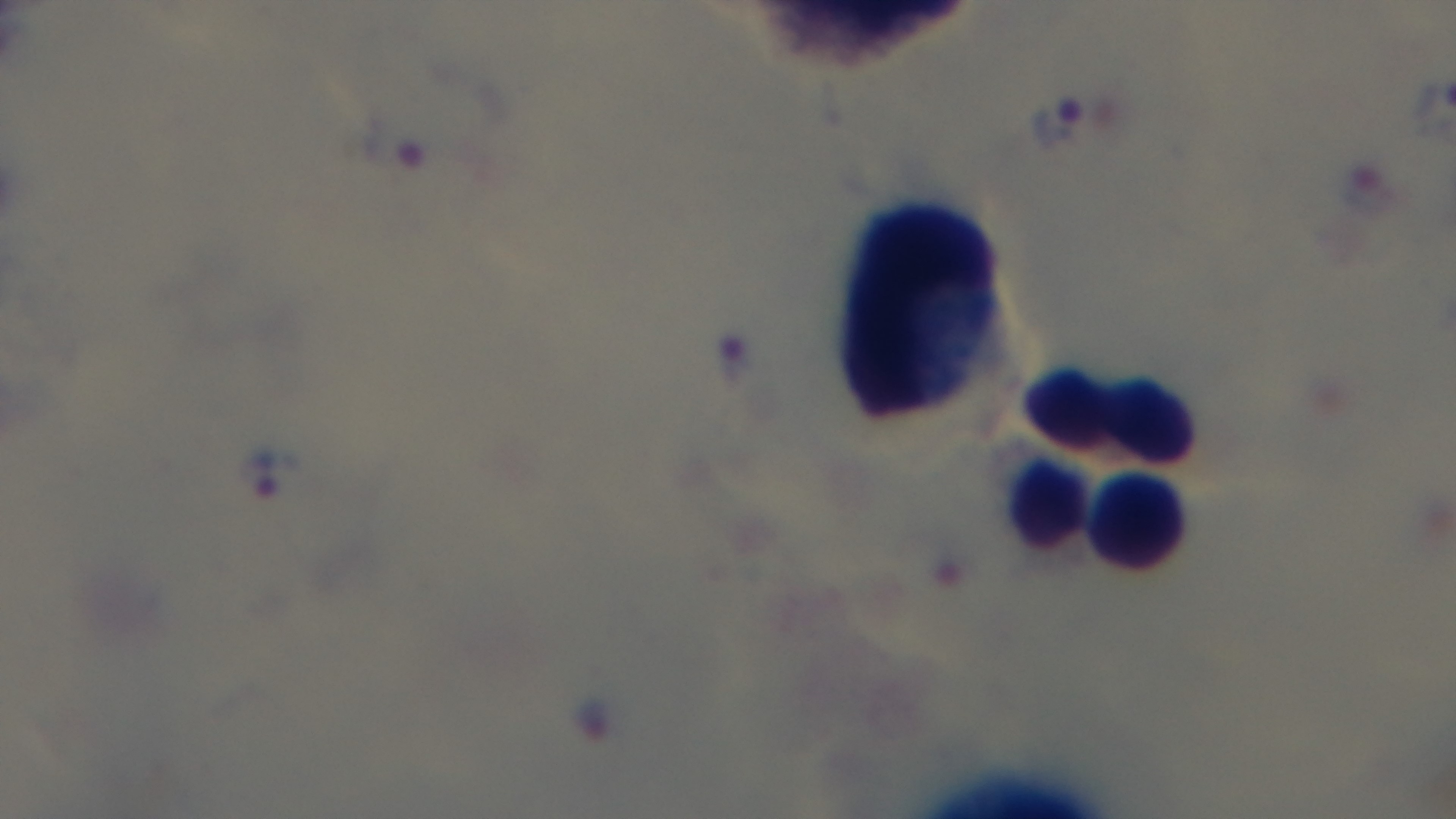

{
  "modality": "light microscopy",
  "stain": "Giemsa",
  "preparation": "thick blood film",
  "malaria_status": "infected",
  "objective": "100x oil immersion",
  "field_of_view": "single",
  "capture": "mounted 4K digital camera"
}